Report the malaria status of this cell.
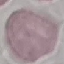

It is uninfected.

Automatically extracted cell patch, resized to 64 × 64 pixels. Giemsa stain. Thin blood smear. Acquired by smartphone through the microscope eyepiece.